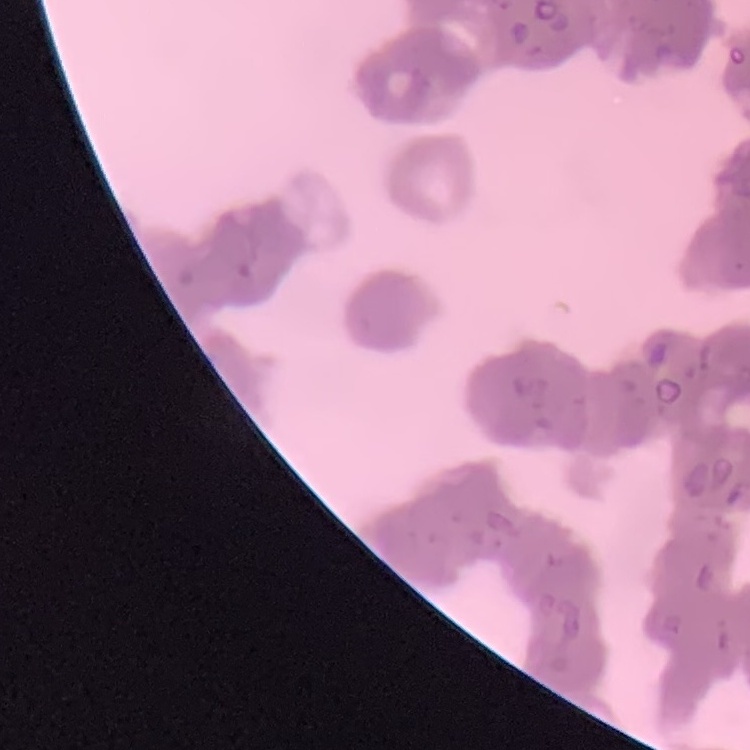
erythrocyte morphology = rouleaux formation
preparation = thin blood smear
stain = Field's or Giemsa
image type = square crop of a larger photomicrograph